Assess this cell for malaria.
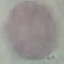

It is uninfected.

Thin smear of blood. Photographed with a smartphone camera at the microscope eyepiece. Giemsa-stained preparation. Cell patch, automatically extracted from a larger field of view and resized to 64 × 64 pixels.